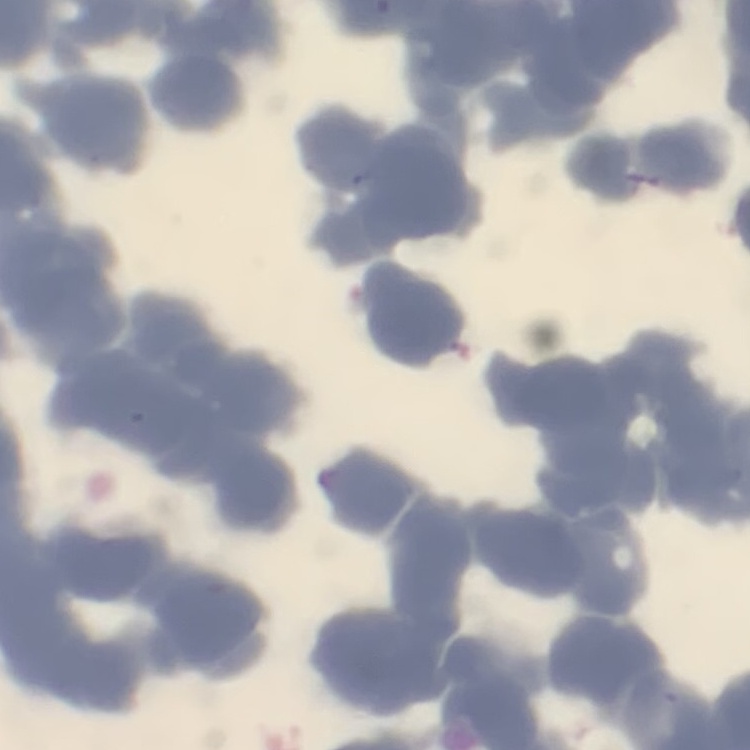
erythrocyte_morphology: rouleaux formation
preparation: thin peripheral smear
image_type: one tile cut from a larger photomicrograph
stain: Field's or Giemsa